Give the position of every Plasmodium parasite and every leukocyte.
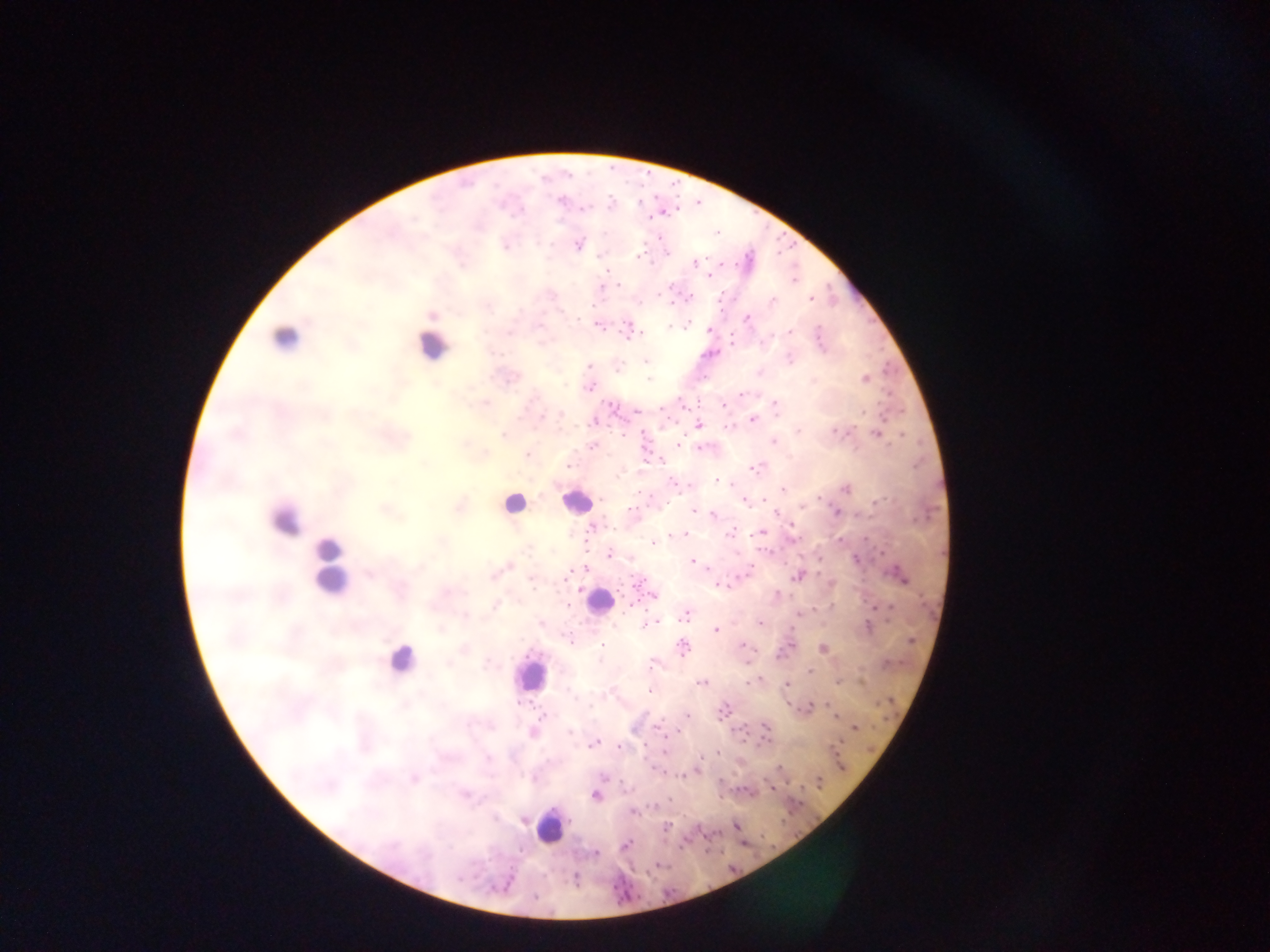
Approximate centers as [x, y] in pixels.
Plasmodium parasites (some below the resolvable threshold): [643, 178], [559, 200], [611, 204], [640, 206], [696, 207], [583, 209], [660, 212], [715, 233], [578, 244], [600, 255], [750, 255], [639, 256], [693, 262], [709, 274], [794, 281], [600, 287], [670, 287], [688, 297], [811, 298], [433, 314], [746, 318], [598, 325], [685, 326], [710, 330], [628, 331], [731, 342], [818, 346], [712, 353], [645, 361], [589, 367], [865, 378], [589, 387], [742, 393], [775, 405], [683, 406], [900, 411], [752, 420], [593, 422], [698, 425], [839, 432], [502, 433], [878, 434], [904, 435], [773, 440], [678, 445], [591, 446], [700, 447], [526, 455], [661, 460], [568, 466], [919, 467], [756, 468], [717, 481], [783, 488], [846, 488], [744, 501], [870, 504], [459, 506], [631, 511], [695, 511], [774, 512], [835, 512], [712, 515], [917, 523], [760, 532], [684, 534], [730, 534], [676, 535], [585, 537], [800, 541], [864, 542], [653, 543], [836, 543], [608, 554], [693, 560], [860, 565], [507, 567], [585, 569], [747, 572], [798, 575], [899, 576], [823, 577], [718, 584], [636, 587], [653, 596], [831, 603], [630, 605], [877, 606], [797, 614], [684, 615], [651, 622], [758, 622], [541, 623], [867, 627], [715, 629], [914, 632], [571, 641], [742, 645], [789, 645], [601, 646], [682, 646], [823, 648], [903, 657], [808, 671], [757, 680], [701, 682], [787, 684], [839, 684], [864, 685], [649, 691], [787, 700], [893, 700], [807, 708], [722, 711], [685, 715], [835, 717], [657, 727], [735, 727], [855, 727], [765, 728], [534, 732], [746, 741], [594, 744], [831, 746], [618, 747], [871, 747], [663, 750], [718, 752], [649, 765], [780, 767], [696, 770], [670, 776], [413, 779], [819, 782], [772, 787], [595, 795], [720, 797], [633, 812], [524, 819], [666, 826], [736, 826], [625, 845], [774, 847], [595, 853], [730, 863].
Leukocytes: [284, 339], [431, 345], [576, 500], [513, 504], [284, 519], [330, 564], [598, 602], [401, 660], [530, 674], [549, 827].

Summary:
  - Capture: mobile-phone photograph through a microscope
  - Country: Ghana
  - Field of view: single
  - Preparation: thick blood film
  - Image size: 1270×952 pixels